State which cell type is depicted.
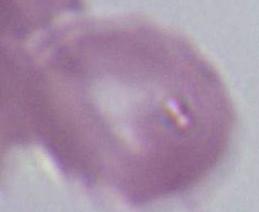

This is an erythrocyte.

magnification: 1000x
modality: photomicrograph